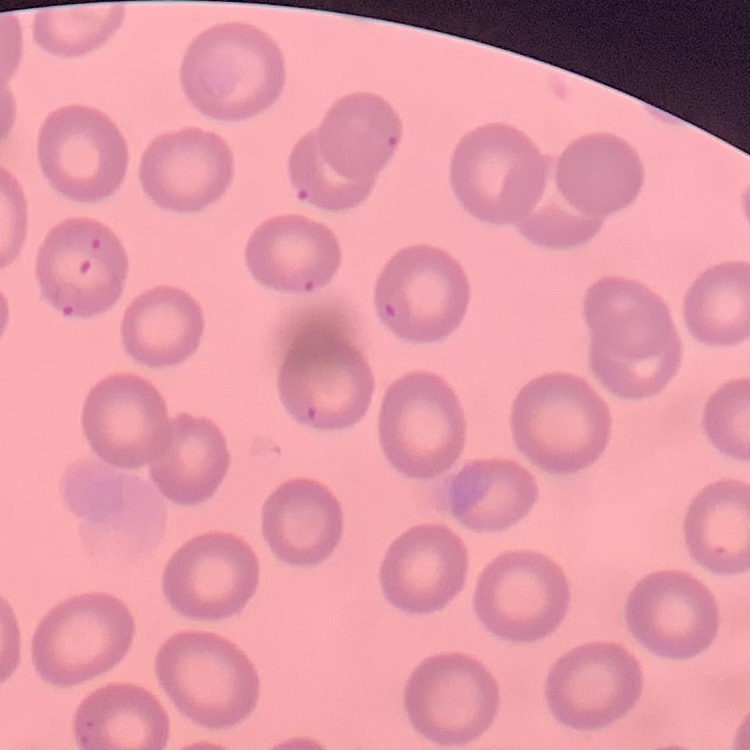 The erythrocytes exhibit no rouleaux formation. Thin blood film. Square crop of a larger photomicrograph. Stained with either Field's or Giemsa.